Report the malaria status of this cell.
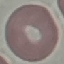
Uninfected.

Summary:
  - Preparation: thin blood film
  - Image type: cell patch, automatically extracted from a larger field of view and resized to 64 × 64 pixels
  - Stain: Giemsa
  - Capture: smartphone camera at the microscope eyepiece